Describe the morphology of the red blood cells.
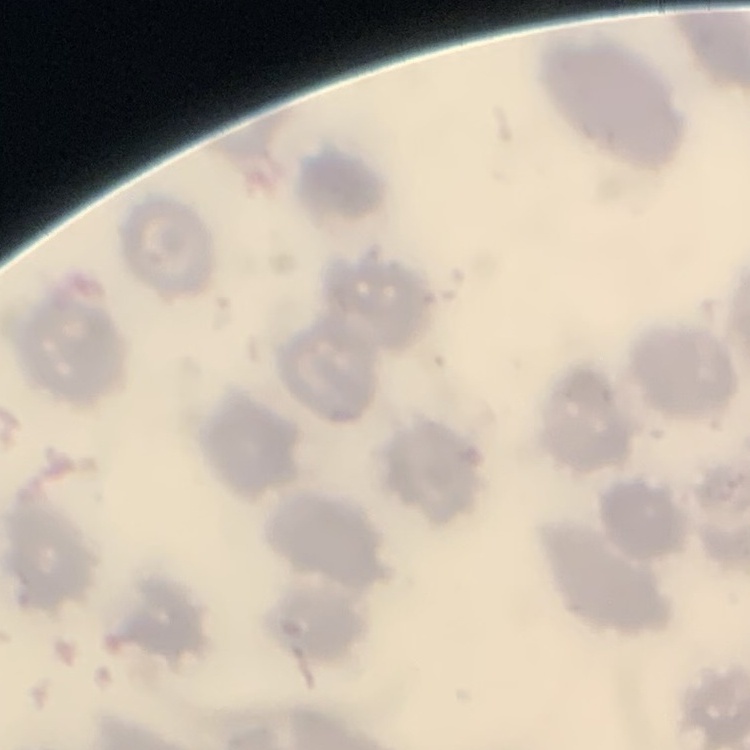

They show no rouleaux formation.

stain = Field's or Giemsa
preparation = thin blood smear
image type = one tile cut from a larger photomicrograph